Classify this cell by malaria status.
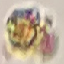

Uninfected.

Cell patch, automatically extracted from a larger field of view and resized to 64 × 64 pixels. Thin blood smear. Photographed with a smartphone camera at the microscope eyepiece. Giemsa stain.